Find the red blood cells and label each as P. falciparum-infected, uninfected, or of indeterminate infection status.
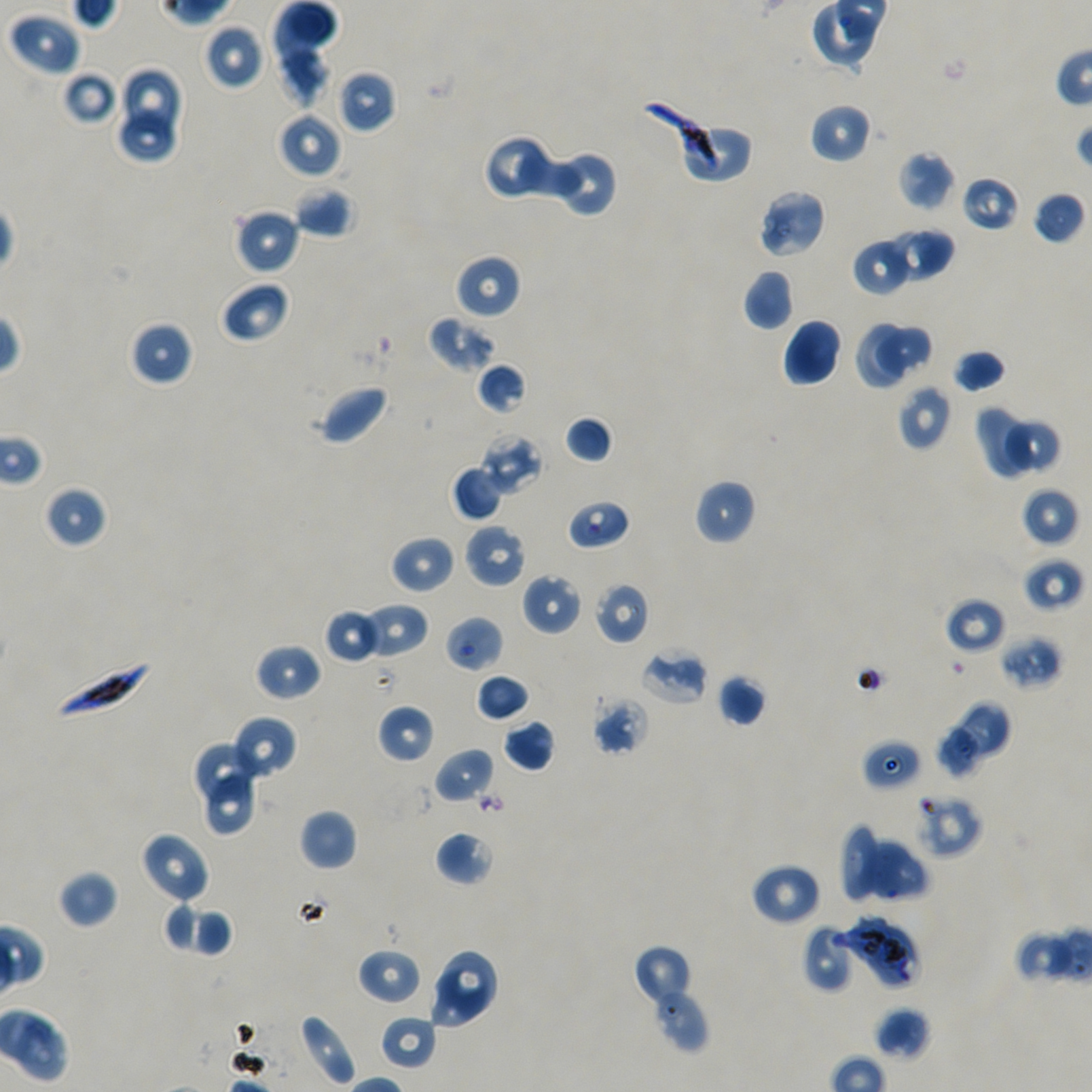
Approximate bounding boxes as {x1, y1, x2, y2} in pixels. Not every red blood cell is marked.
Infected red blood cells: {52, 658, 151, 724}.
Red blood cells of indeterminate infection status: {641, 98, 725, 173}, {566, 498, 632, 551}, {594, 581, 650, 645}, {444, 615, 504, 673}, {862, 738, 922, 790}, {913, 792, 982, 858}, {843, 916, 920, 991}.
Uninfected red blood cells: {9, 12, 81, 76}, {203, 24, 265, 91}, {275, 44, 333, 109}, {122, 67, 183, 136}, {338, 70, 397, 133}, {62, 71, 117, 125}, {809, 103, 872, 164}, {277, 112, 342, 179}, {117, 113, 179, 165}, {682, 124, 752, 184}, {483, 135, 550, 201}, {513, 143, 583, 202}, {547, 148, 619, 217}, {898, 150, 955, 212}, {961, 175, 1021, 232}, {293, 185, 356, 238}, {756, 188, 826, 259}, {1032, 191, 1085, 245}, {233, 208, 301, 275}, {889, 227, 954, 282}, {852, 237, 913, 296}, {454, 254, 522, 320}, {742, 268, 795, 331}, {221, 280, 291, 344}, {426, 314, 496, 373}, {783, 318, 842, 387}, {130, 321, 194, 387}, {854, 321, 908, 390}, {875, 323, 934, 380}, {952, 348, 1006, 393}, {477, 362, 527, 415}, {312, 383, 391, 446}, {897, 384, 951, 451}, {975, 407, 1029, 479}, {564, 415, 614, 464}, {1004, 418, 1060, 476}, {481, 433, 541, 494}, {451, 464, 506, 522}, {694, 479, 756, 545}, {43, 484, 107, 549}, {1021, 487, 1079, 547}, {463, 523, 528, 588}, {390, 534, 456, 595}, {1022, 557, 1084, 613}, {522, 572, 582, 636}, {943, 596, 1006, 655}, {363, 602, 430, 659}, {323, 608, 382, 664}, {999, 635, 1063, 690}, {253, 643, 322, 703}, {640, 646, 708, 706}, {475, 673, 530, 723}, {717, 674, 767, 727}, {592, 697, 650, 757}, {949, 699, 1012, 762}, {377, 704, 435, 763}, {230, 716, 296, 780}, {503, 719, 556, 772}, {932, 726, 983, 781}, {194, 740, 263, 803}, {433, 747, 495, 805}, {205, 771, 257, 839}, {299, 809, 357, 871}, {839, 824, 881, 904}, {435, 829, 496, 887}, {139, 831, 211, 905}, {856, 835, 930, 904}, {750, 862, 822, 926}, {57, 869, 118, 928}, {162, 901, 197, 954}, {189, 908, 234, 962}, {803, 924, 856, 992}, {1014, 926, 1074, 983}, {632, 945, 695, 1010}, {357, 947, 421, 1005}, {434, 951, 497, 1019}, {428, 967, 490, 1028}, {647, 978, 710, 1055}, {875, 1006, 932, 1060}, {297, 1013, 357, 1087}, {380, 1015, 438, 1071}.

objective: 100x, oil immersion, numerical aperture 1.45
field_of_view: single
donor_blood_group: A+/O+
stain: Giemsa
preparation: thin blood film
culture: P. falciparum strain NF54, static, in vitro
image_size: 1092×1092 pixels